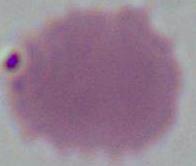
An erythrocyte is shown. Captured at 1000x magnification. Photomicrograph.